Outline each blood parasite and name the species.
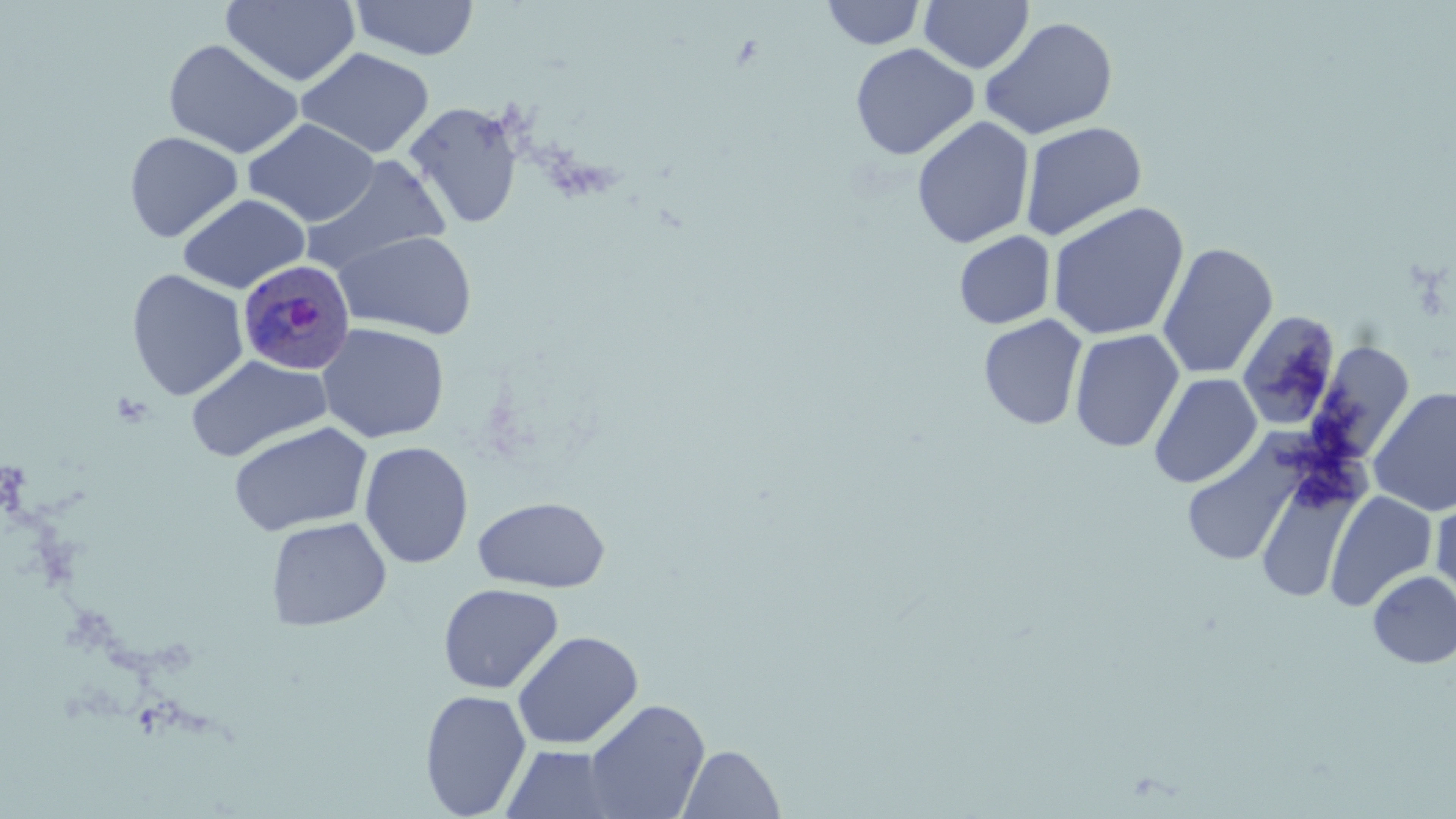
Approximate bounding boxes as (x1, y1, x2, y2) in pixels.
Plasmodium ovale-infected red blood cells: (237, 259, 356, 376).
No Plasmodium falciparum, Plasmodium malariae, Plasmodium vivax, Babesia divergens, or Trypanosoma brucei observed.

Summary:
  - Uninfected red blood cell locations: (220, 0, 362, 87), (351, 0, 479, 61), (820, 0, 928, 50), (919, 0, 1034, 74), (980, 15, 1119, 140), (163, 38, 304, 160), (849, 43, 979, 161), (296, 47, 434, 159), (403, 101, 525, 231), (911, 116, 1035, 249), (243, 118, 380, 226), (1019, 121, 1147, 240), (124, 131, 243, 243), (299, 154, 452, 277), (177, 193, 310, 294), (1046, 201, 1189, 341), (333, 230, 478, 339), (954, 230, 1056, 329), (1157, 242, 1278, 380), (126, 269, 249, 401), (1235, 311, 1342, 432), (977, 314, 1088, 431), (316, 322, 450, 444), (1069, 328, 1184, 452), (1303, 340, 1417, 468), (186, 354, 332, 462), (1148, 373, 1263, 489), (1368, 386, 1456, 516), (228, 421, 373, 537), (1181, 435, 1307, 568), (358, 441, 474, 569), (1254, 473, 1362, 604), (1325, 491, 1438, 612), (1432, 492, 1456, 612), (473, 495, 611, 592), (265, 516, 392, 631), (1367, 571, 1456, 668), (437, 583, 564, 694), (511, 630, 644, 749), (420, 689, 532, 818), (583, 699, 711, 818), (498, 744, 631, 819), (677, 744, 785, 819)
  - Slide-level diagnosis: Plasmodium ovale
  - Modality: optical microscopy
  - Stain: May-Grünwald-Giemsa
  - Image size: 1456×819 pixels
  - Magnification: 1000x
  - Preparation: thin blood film
  - Field of view: one of a larger specimen